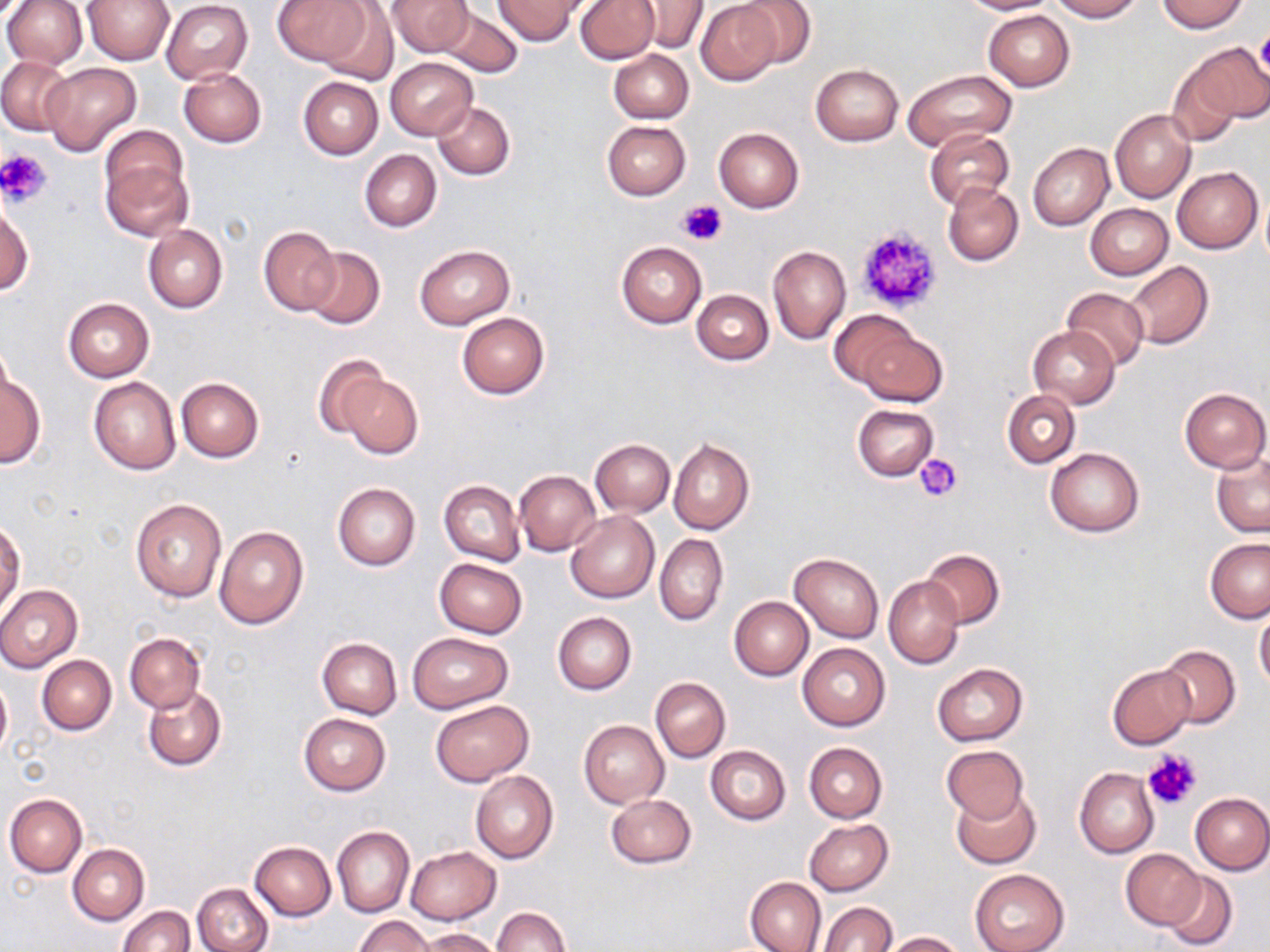

Summary:
  - Coordinate format: approximate bounding boxes as (x1, y1, x2, y2) in pixels
  - Platelet locations: (1255, 28, 1270, 84), (0, 148, 53, 206), (678, 198, 725, 245), (853, 226, 943, 315), (915, 453, 963, 503), (1140, 746, 1203, 811)
  - Uninfected red blood cell locations: (83, 0, 173, 63), (274, 0, 370, 67), (387, 0, 475, 58), (576, 0, 659, 63), (733, 0, 816, 68), (958, 0, 1058, 15), (1047, 0, 1143, 21), (1155, 0, 1250, 33), (1, 1, 87, 69), (161, 1, 253, 84), (495, 1, 583, 44), (316, 2, 399, 85), (633, 2, 707, 54), (697, 2, 782, 84), (437, 4, 522, 76), (983, 11, 1075, 90), (1180, 42, 1269, 132), (609, 50, 693, 123), (0, 56, 72, 135), (385, 58, 477, 138), (1165, 61, 1245, 148), (40, 63, 141, 155), (811, 64, 903, 146), (179, 67, 266, 147), (903, 70, 1016, 152), (298, 76, 383, 159), (402, 76, 500, 171), (433, 100, 514, 180), (1110, 109, 1195, 203), (602, 120, 690, 199), (100, 124, 187, 212), (713, 128, 803, 213), (924, 128, 1014, 211), (1027, 143, 1114, 230), (360, 149, 442, 231), (101, 156, 193, 243), (1172, 167, 1263, 252), (943, 183, 1024, 266), (1, 197, 32, 295), (1087, 204, 1173, 280), (144, 224, 228, 313), (259, 226, 340, 315), (616, 241, 707, 327), (414, 244, 515, 328), (768, 245, 851, 344), (302, 247, 385, 329), (1126, 261, 1213, 348), (1062, 287, 1149, 371), (692, 289, 773, 365), (63, 299, 154, 381), (829, 310, 921, 392), (457, 312, 549, 399), (853, 325, 946, 406), (1028, 326, 1121, 407), (0, 346, 15, 417), (313, 354, 391, 439), (328, 366, 422, 458), (0, 375, 45, 467), (88, 376, 180, 474), (176, 377, 264, 462), (1180, 387, 1269, 472), (1002, 390, 1081, 468), (853, 404, 937, 480), (669, 439, 753, 534), (590, 440, 675, 516), (1045, 447, 1144, 536), (1211, 454, 1270, 538), (515, 470, 602, 556), (439, 479, 525, 566), (333, 484, 421, 571), (130, 498, 227, 602), (566, 512, 659, 603), (1, 520, 24, 613), (214, 524, 309, 630), (655, 532, 728, 626), (1205, 538, 1270, 624), (920, 549, 1004, 629), (789, 554, 884, 643), (434, 558, 528, 638), (884, 576, 962, 668), (0, 585, 82, 672), (729, 596, 814, 680), (1254, 607, 1270, 691), (553, 613, 636, 695), (124, 632, 205, 713), (408, 632, 513, 713), (317, 637, 402, 718), (798, 643, 890, 730), (1155, 644, 1239, 728), (37, 655, 116, 735), (932, 662, 1028, 746), (1107, 663, 1197, 750), (0, 675, 11, 760), (650, 677, 731, 762), (144, 685, 227, 771), (430, 699, 533, 786), (298, 713, 391, 796), (578, 720, 668, 809), (803, 742, 886, 823), (706, 746, 791, 824), (942, 746, 1029, 824), (1074, 768, 1159, 858), (470, 770, 559, 863), (951, 787, 1041, 868), (1190, 792, 1270, 874), (4, 794, 86, 878), (605, 794, 697, 868), (804, 819, 893, 895), (332, 825, 415, 917), (249, 841, 336, 920), (67, 844, 148, 925), (406, 846, 501, 924), (1120, 849, 1205, 931), (970, 869, 1069, 952), (1160, 871, 1238, 951), (745, 876, 827, 952), (192, 882, 273, 952), (819, 902, 897, 952), (119, 905, 194, 952), (493, 907, 571, 952), (354, 915, 435, 952), (421, 928, 504, 952), (882, 931, 963, 951)
  - Slide-level diagnosis: no evidence of blood parasites
  - Field of view: single
  - Preparation: thin blood smear
  - Magnification: 1000x
  - Image size: 1270×952 pixels
  - Stain: May-Grünwald-Giemsa
  - Modality: light microscopy